Report the malaria status of this cell.
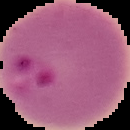

Parasitized.

image size = 130×130 pixels
preparation = thin blood film
image type = segmented cell region with the area outside set to black